Report the malaria status of this cell.
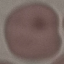
Uninfected.

stain = Giemsa
image type = automatically extracted cell patch, resized to 64 × 64 pixels
preparation = thin blood film
capture = smartphone camera at the microscope eyepiece